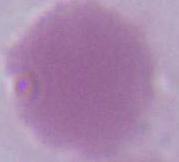

identification = erythrocyte
modality = micrograph
magnification = 1000x